Identify the blood parasite species.
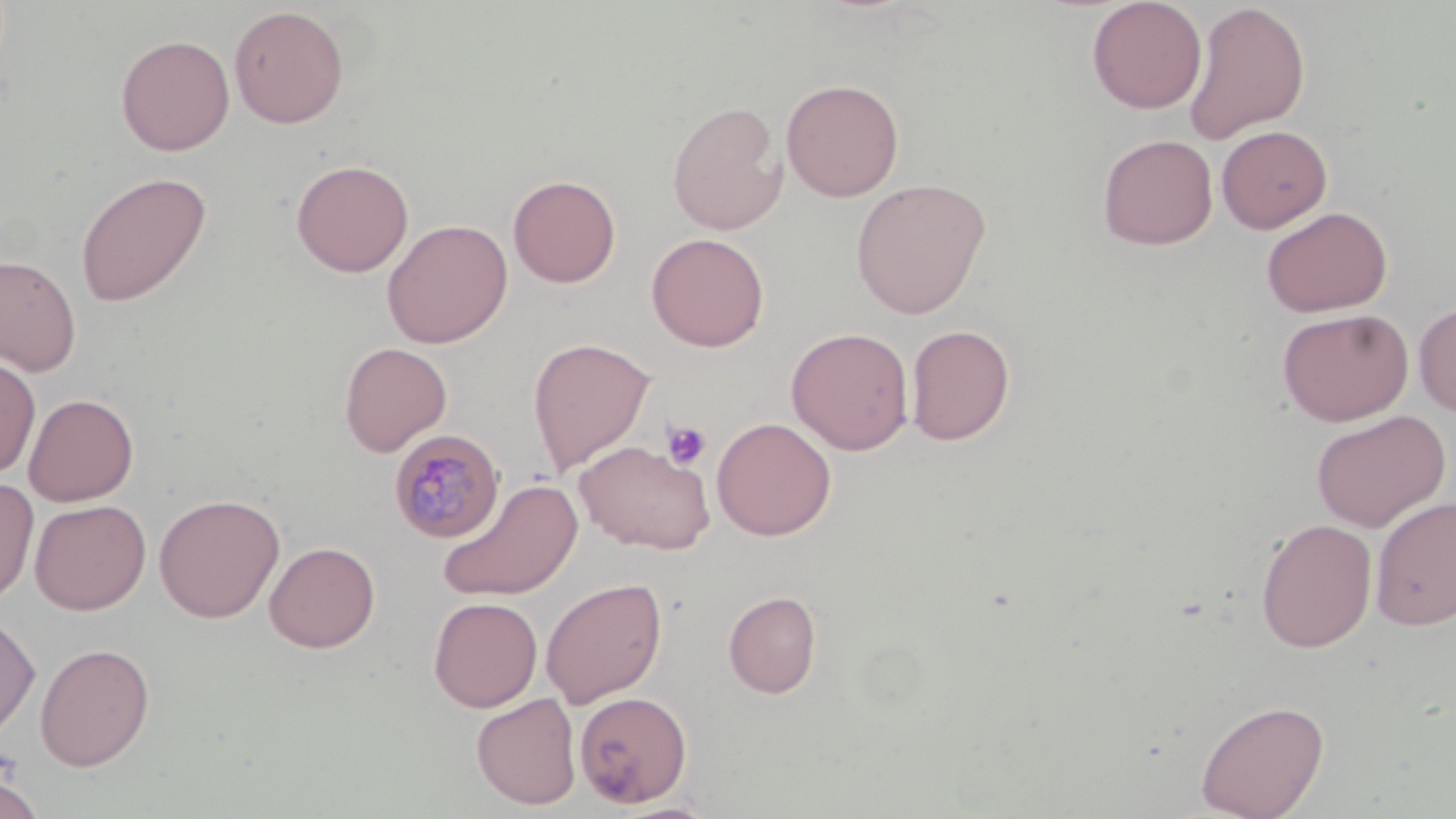

Plasmodium malariae.

Approximate bounding boxes as (x1,y1)-(x2,y2) corner pairs in pixels. Platelet locations: (661,420)-(712,472). Plasmodium malariae-infected red blood cell locations: (389,429)-(505,543). Uninfected red blood cell locations: (1087,0)-(1207,114), (1184,2)-(1311,145), (229,5)-(349,128), (116,34)-(235,155), (781,78)-(904,202), (666,101)-(788,235), (1216,125)-(1332,233), (1097,134)-(1218,250), (290,158)-(414,277), (75,171)-(212,307), (508,174)-(621,288), (851,177)-(992,319), (1261,206)-(1393,317), (381,218)-(513,348), (646,233)-(769,352), (0,253)-(81,376), (1413,301)-(1456,416), (1277,307)-(1414,426), (905,324)-(1016,446), (786,327)-(914,455), (527,337)-(656,477), (339,342)-(452,456), (0,355)-(41,479), (23,393)-(139,506), (1311,410)-(1451,532), (711,417)-(837,541), (574,440)-(715,555), (0,477)-(39,606), (437,478)-(583,602), (154,493)-(285,623), (1370,495)-(1456,631), (29,499)-(151,614), (1255,518)-(1377,653), (264,541)-(381,653), (540,577)-(668,709), (723,590)-(822,698), (428,597)-(543,712), (0,611)-(40,741), (34,642)-(155,771), (574,690)-(693,807), (471,692)-(582,809), (1195,698)-(1330,819), (0,772)-(45,819), (603,799)-(724,818). Image is 1456×819 pixels. Light microscopy. May-Grünwald-Giemsa stain. Thin blood smear. 1000x magnification. One field of a larger specimen.